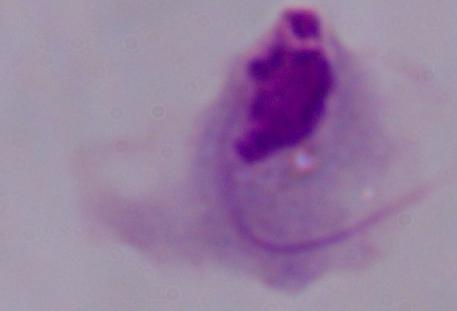

Summary:
  - Identification: trichomonad
  - Modality: micrograph
  - Magnification: 1000x